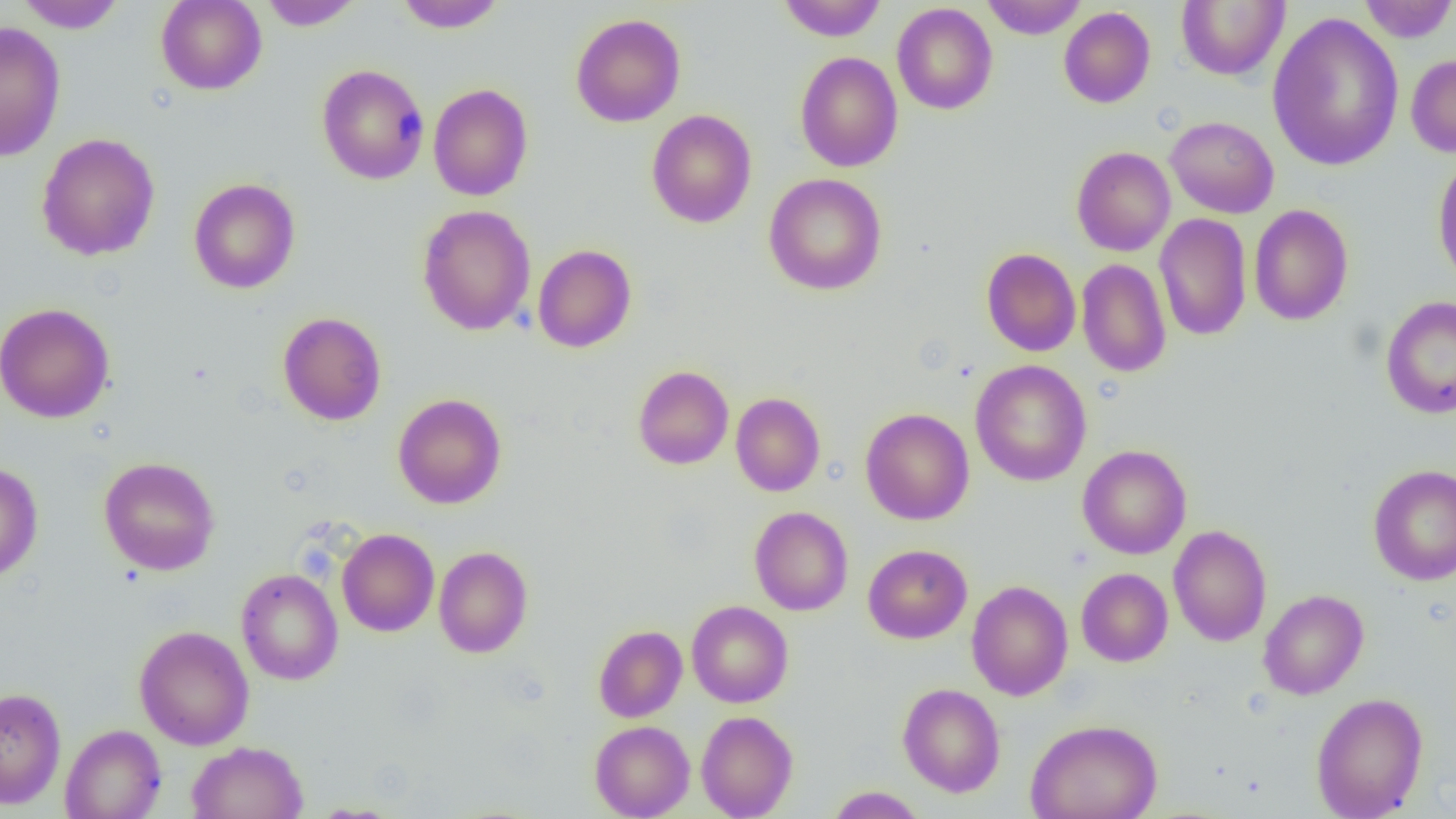

slide-level diagnosis = negative for blood parasites
image size = 1456×819 pixels
magnification = 1000x
preparation = thin blood smear
field of view = one of a larger specimen
modality = light microscopy
uninfected red blood cell locations = approximate bounding boxes as [x1, y1, x2, y2] in pixels: [15, 0, 126, 33], [156, 0, 266, 95], [394, 0, 507, 32], [778, 0, 887, 42], [981, 0, 1087, 39], [1177, 0, 1289, 81], [1357, 0, 1456, 43], [258, 1, 362, 30], [892, 3, 998, 115], [1059, 7, 1155, 108], [1266, 11, 1404, 172], [570, 13, 686, 127], [0, 21, 66, 162], [795, 51, 903, 172], [1406, 53, 1456, 158], [316, 64, 429, 184], [428, 83, 533, 201], [646, 109, 757, 228], [1165, 116, 1279, 218], [36, 133, 160, 261], [1071, 146, 1175, 256], [1432, 155, 1456, 289], [764, 173, 887, 296], [188, 178, 300, 294], [1248, 204, 1354, 325], [417, 205, 536, 335], [1154, 212, 1252, 341], [414, 231, 636, 343], [533, 244, 636, 352], [981, 247, 1081, 356], [1077, 259, 1172, 377], [1380, 294, 1456, 419], [0, 302, 115, 423], [277, 311, 386, 425], [970, 359, 1092, 486], [633, 365, 734, 469], [731, 392, 826, 496], [393, 393, 507, 509], [860, 408, 974, 525], [1078, 445, 1191, 559], [99, 456, 220, 576], [0, 462, 44, 583], [1368, 464, 1456, 586], [749, 506, 853, 615], [1169, 524, 1272, 646], [337, 528, 439, 636], [863, 544, 972, 644], [433, 546, 533, 658], [236, 568, 343, 685], [1076, 568, 1173, 666], [967, 580, 1073, 700], [1258, 589, 1369, 700], [686, 601, 793, 707], [593, 625, 687, 722], [135, 626, 254, 750], [898, 683, 1006, 797], [0, 687, 66, 809], [1310, 692, 1428, 818], [696, 710, 798, 819], [1025, 718, 1163, 819], [590, 720, 695, 819], [60, 724, 167, 819], [186, 741, 308, 819], [825, 786, 927, 818]